Report the malaria status.
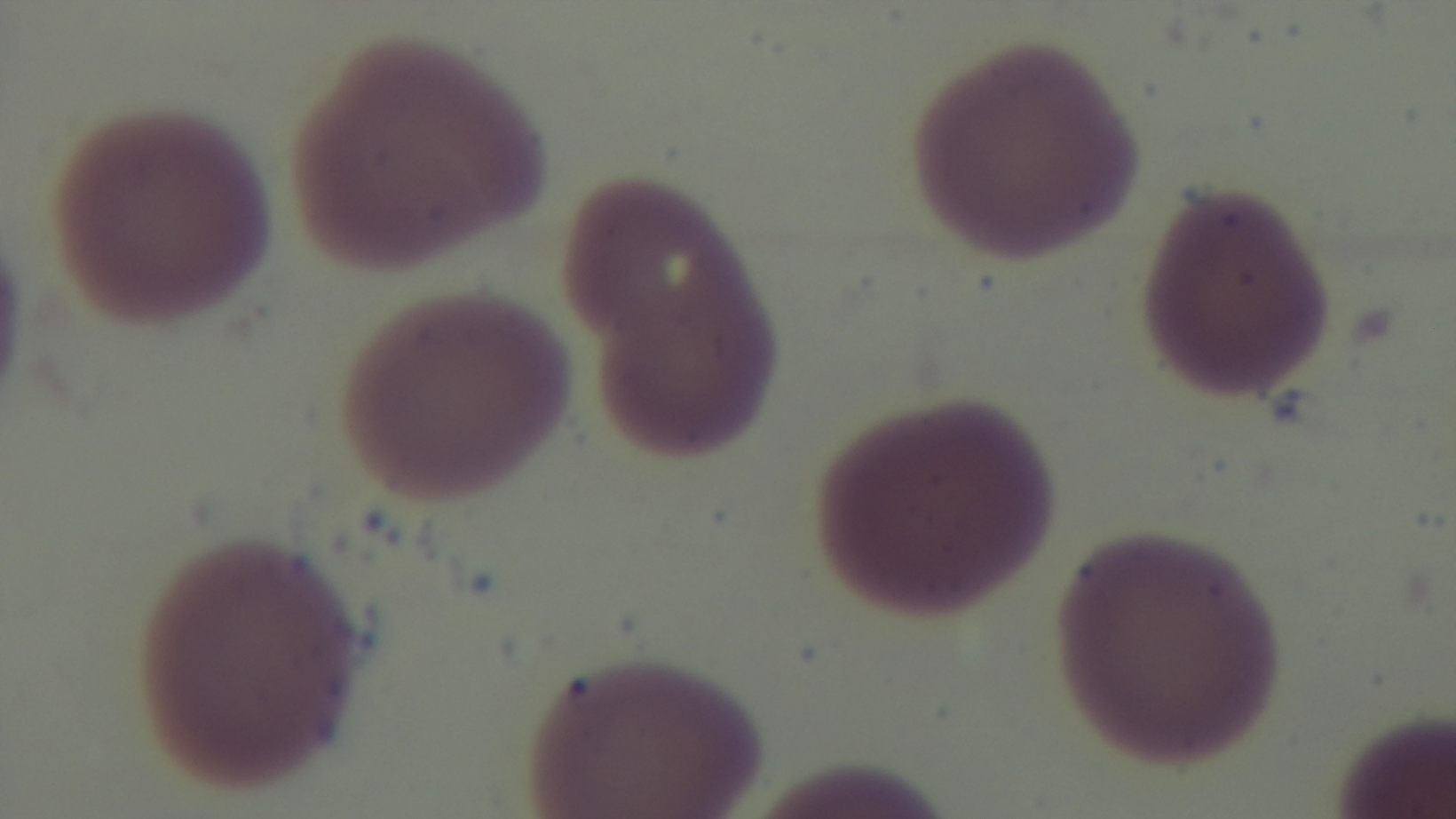

Negative.

Captured with a mounted 4K digital camera. One field from the slide. Preparation: thin smear. Oil-immersion objective, 100x. Giemsa stain. Photomicrograph.